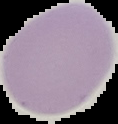
preparation = thin blood smear
image type = segmented cell region on a black background
malaria status = uninfected
image size = 118×124 pixels